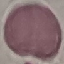
result = no malaria parasites detected
image type = automatically extracted cell patch, resized to 64 × 64 pixels
preparation = thin blood film
stain = Giemsa
capture = smartphone camera at the microscope eyepiece